Report the malaria status of this cell.
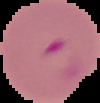

It is parasitized.

image size = 100×103 pixels
preparation = thin blood smear
image type = cell region segmented out of the field of view; surrounding area masked to black